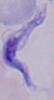

Summary:
  - Modality: micrograph
  - Identification: trypanosome
  - Magnification: 1000x